Describe the morphology of the red blood cells.
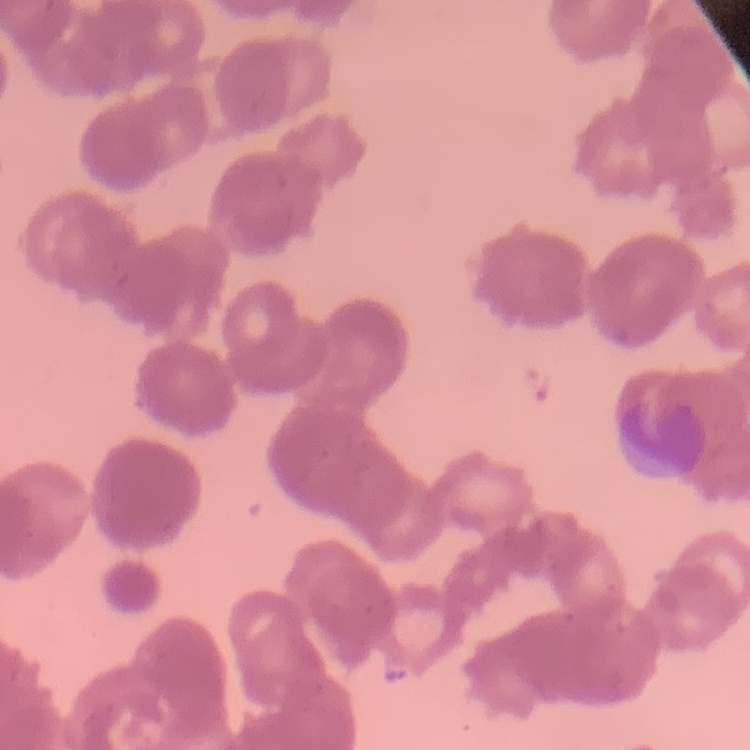
Rouleaux formation.

Summary:
  - Preparation: thin blood smear
  - Stain: Field's or Giemsa
  - Image type: square crop of a larger photomicrograph